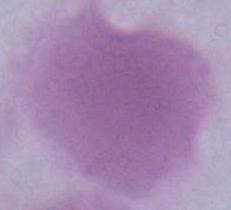 1000x magnification. Photomicrograph. An erythrocyte is seen.